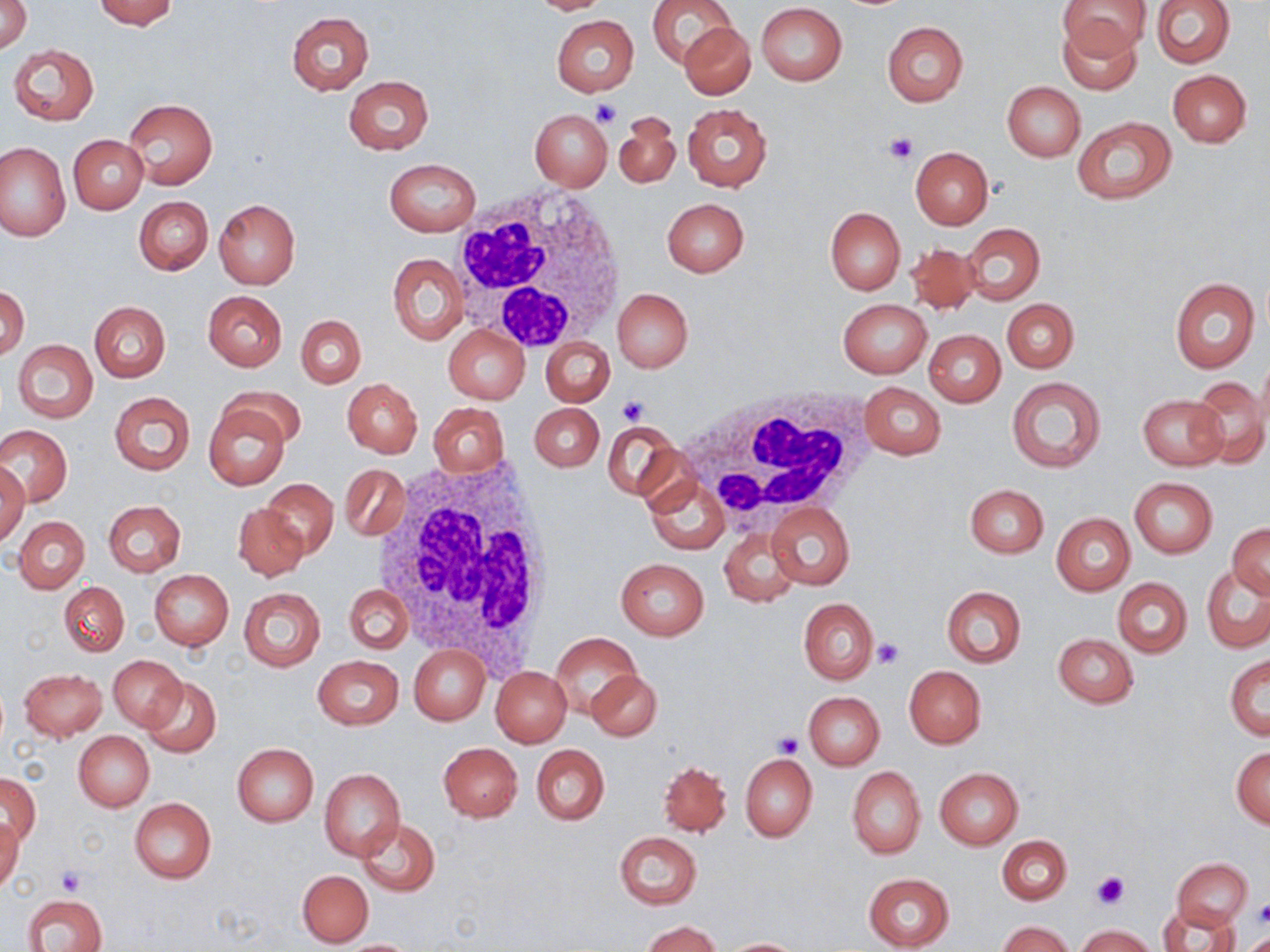
Summary:
  - Coordinate format: approximate bounding boxes as named x1/y1/x2/y2 corners in pixels
  - Uninfected red blood cell locations: (x1=1, y1=0, x2=31, y2=53), (x1=92, y1=0, x2=179, y2=29), (x1=523, y1=0, x2=614, y2=14), (x1=647, y1=0, x2=736, y2=70), (x1=1150, y1=0, x2=1236, y2=67), (x1=1058, y1=2, x2=1151, y2=57), (x1=756, y1=3, x2=847, y2=85), (x1=287, y1=12, x2=373, y2=94), (x1=1054, y1=14, x2=1144, y2=95), (x1=551, y1=15, x2=640, y2=96), (x1=883, y1=21, x2=968, y2=106), (x1=682, y1=22, x2=755, y2=99), (x1=8, y1=44, x2=99, y2=124), (x1=1167, y1=69, x2=1252, y2=147), (x1=343, y1=75, x2=434, y2=154), (x1=1002, y1=82, x2=1084, y2=160), (x1=122, y1=99, x2=218, y2=189), (x1=682, y1=103, x2=771, y2=191), (x1=529, y1=110, x2=612, y2=190), (x1=613, y1=112, x2=680, y2=188), (x1=1071, y1=116, x2=1177, y2=203), (x1=68, y1=135, x2=148, y2=214), (x1=0, y1=140, x2=69, y2=241), (x1=909, y1=146, x2=993, y2=229), (x1=384, y1=158, x2=480, y2=236), (x1=134, y1=196, x2=213, y2=275), (x1=661, y1=197, x2=749, y2=278), (x1=213, y1=199, x2=300, y2=289), (x1=825, y1=207, x2=905, y2=294), (x1=961, y1=223, x2=1044, y2=306), (x1=905, y1=242, x2=981, y2=314), (x1=388, y1=253, x2=467, y2=344), (x1=1169, y1=276, x2=1259, y2=374), (x1=1, y1=287, x2=28, y2=360), (x1=613, y1=289, x2=693, y2=373), (x1=203, y1=291, x2=287, y2=371), (x1=837, y1=299, x2=932, y2=377), (x1=1003, y1=299, x2=1078, y2=373), (x1=90, y1=301, x2=170, y2=382), (x1=296, y1=315, x2=365, y2=387), (x1=444, y1=325, x2=529, y2=403), (x1=924, y1=330, x2=1005, y2=406), (x1=541, y1=337, x2=615, y2=407), (x1=13, y1=340, x2=98, y2=423), (x1=1005, y1=376, x2=1106, y2=474), (x1=1187, y1=376, x2=1270, y2=467), (x1=343, y1=378, x2=422, y2=457), (x1=857, y1=382, x2=947, y2=458), (x1=218, y1=384, x2=307, y2=448), (x1=109, y1=392, x2=195, y2=474), (x1=1138, y1=396, x2=1226, y2=470), (x1=203, y1=402, x2=290, y2=491), (x1=429, y1=403, x2=509, y2=476), (x1=530, y1=403, x2=604, y2=471), (x1=603, y1=420, x2=680, y2=501), (x1=1, y1=425, x2=72, y2=506), (x1=0, y1=462, x2=30, y2=542), (x1=341, y1=464, x2=408, y2=541), (x1=645, y1=476, x2=728, y2=553), (x1=1129, y1=477, x2=1218, y2=558), (x1=260, y1=479, x2=339, y2=559), (x1=965, y1=484, x2=1048, y2=558), (x1=104, y1=500, x2=186, y2=576), (x1=767, y1=502, x2=854, y2=590), (x1=233, y1=503, x2=308, y2=580), (x1=1051, y1=513, x2=1135, y2=595), (x1=14, y1=516, x2=89, y2=593), (x1=1228, y1=523, x2=1270, y2=598), (x1=720, y1=527, x2=802, y2=608), (x1=615, y1=557, x2=709, y2=640), (x1=1202, y1=565, x2=1270, y2=653), (x1=149, y1=569, x2=234, y2=650), (x1=1113, y1=577, x2=1192, y2=657), (x1=59, y1=582, x2=128, y2=656), (x1=344, y1=586, x2=412, y2=655), (x1=941, y1=586, x2=1026, y2=667), (x1=238, y1=588, x2=325, y2=672), (x1=798, y1=598, x2=877, y2=684), (x1=550, y1=633, x2=643, y2=716), (x1=1053, y1=633, x2=1139, y2=708), (x1=409, y1=645, x2=489, y2=725), (x1=109, y1=655, x2=187, y2=732), (x1=1225, y1=655, x2=1270, y2=741), (x1=313, y1=656, x2=402, y2=729), (x1=490, y1=665, x2=571, y2=747), (x1=904, y1=665, x2=986, y2=748), (x1=19, y1=667, x2=107, y2=740), (x1=588, y1=668, x2=662, y2=741), (x1=142, y1=676, x2=221, y2=755), (x1=804, y1=692, x2=885, y2=768), (x1=74, y1=731, x2=154, y2=811), (x1=438, y1=742, x2=522, y2=822), (x1=231, y1=743, x2=318, y2=826), (x1=531, y1=744, x2=609, y2=824), (x1=1231, y1=747, x2=1270, y2=828), (x1=740, y1=753, x2=817, y2=841), (x1=659, y1=761, x2=730, y2=836), (x1=847, y1=767, x2=926, y2=859), (x1=935, y1=767, x2=1024, y2=849), (x1=320, y1=768, x2=405, y2=860), (x1=1, y1=771, x2=40, y2=846), (x1=129, y1=797, x2=216, y2=883), (x1=0, y1=816, x2=23, y2=895), (x1=356, y1=818, x2=440, y2=895), (x1=614, y1=831, x2=702, y2=908), (x1=998, y1=835, x2=1072, y2=904), (x1=1173, y1=857, x2=1253, y2=929), (x1=298, y1=870, x2=373, y2=947), (x1=863, y1=873, x2=953, y2=951), (x1=23, y1=893, x2=106, y2=952), (x1=1161, y1=906, x2=1241, y2=952), (x1=644, y1=920, x2=720, y2=952), (x1=1000, y1=921, x2=1071, y2=952), (x1=1077, y1=925, x2=1157, y2=952), (x1=1245, y1=932, x2=1269, y2=951), (x1=720, y1=938, x2=807, y2=951), (x1=335, y1=939, x2=423, y2=951)
  - Platelet locations: (x1=591, y1=98, x2=622, y2=129), (x1=883, y1=131, x2=919, y2=163), (x1=617, y1=395, x2=647, y2=424), (x1=873, y1=638, x2=905, y2=669), (x1=775, y1=732, x2=803, y2=758), (x1=56, y1=867, x2=88, y2=894), (x1=1091, y1=870, x2=1127, y2=908), (x1=1254, y1=901, x2=1270, y2=927)
  - White blood cell locations: (x1=451, y1=184, x2=631, y2=354), (x1=676, y1=382, x2=873, y2=526), (x1=375, y1=457, x2=561, y2=662)
  - Slide-level diagnosis: no evidence of blood parasites
  - Magnification: 1000x
  - Modality: light microscopy
  - Field of view: one of a larger specimen
  - Image size: 1270×952 pixels
  - Preparation: thin blood smear
  - Stain: May-Grünwald-Giemsa